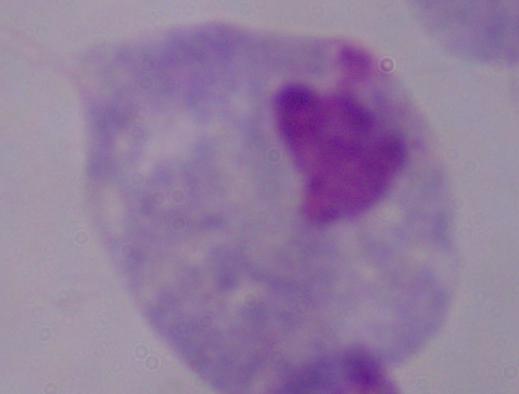
identification = trichomonad
magnification = 1000x
modality = photomicrograph